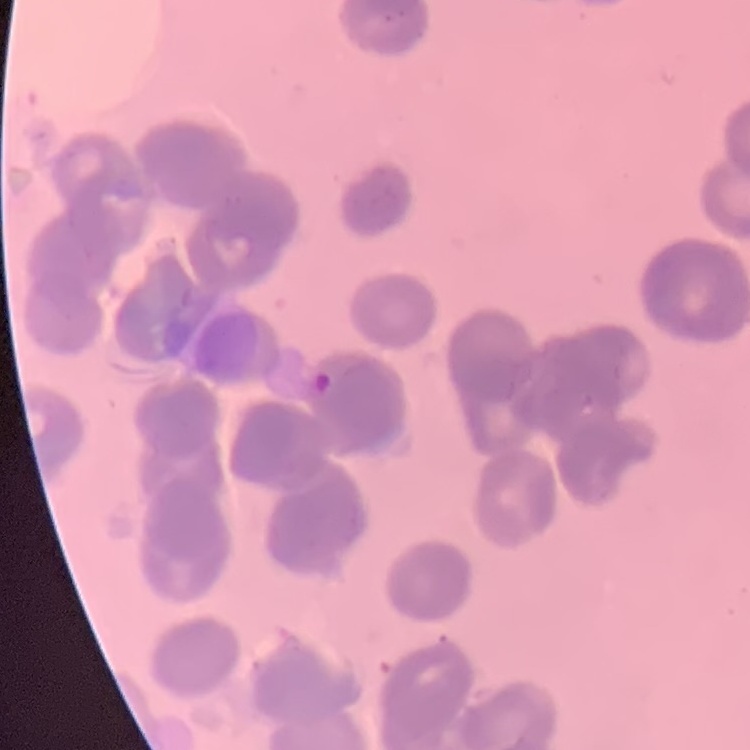
{
  "red_blood_cell_morphology": "rouleaux formation",
  "stain": "Field's or Giemsa",
  "image_type": "one tile cut from a larger photomicrograph",
  "preparation": "thin blood smear"
}